Classify this cell by malaria status.
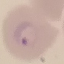

It is parasitized.

preparation = thin smear
image type = automatically extracted cell patch, resized to 64 × 64 pixels
stain = Giemsa
capture = smartphone camera at the microscope eyepiece